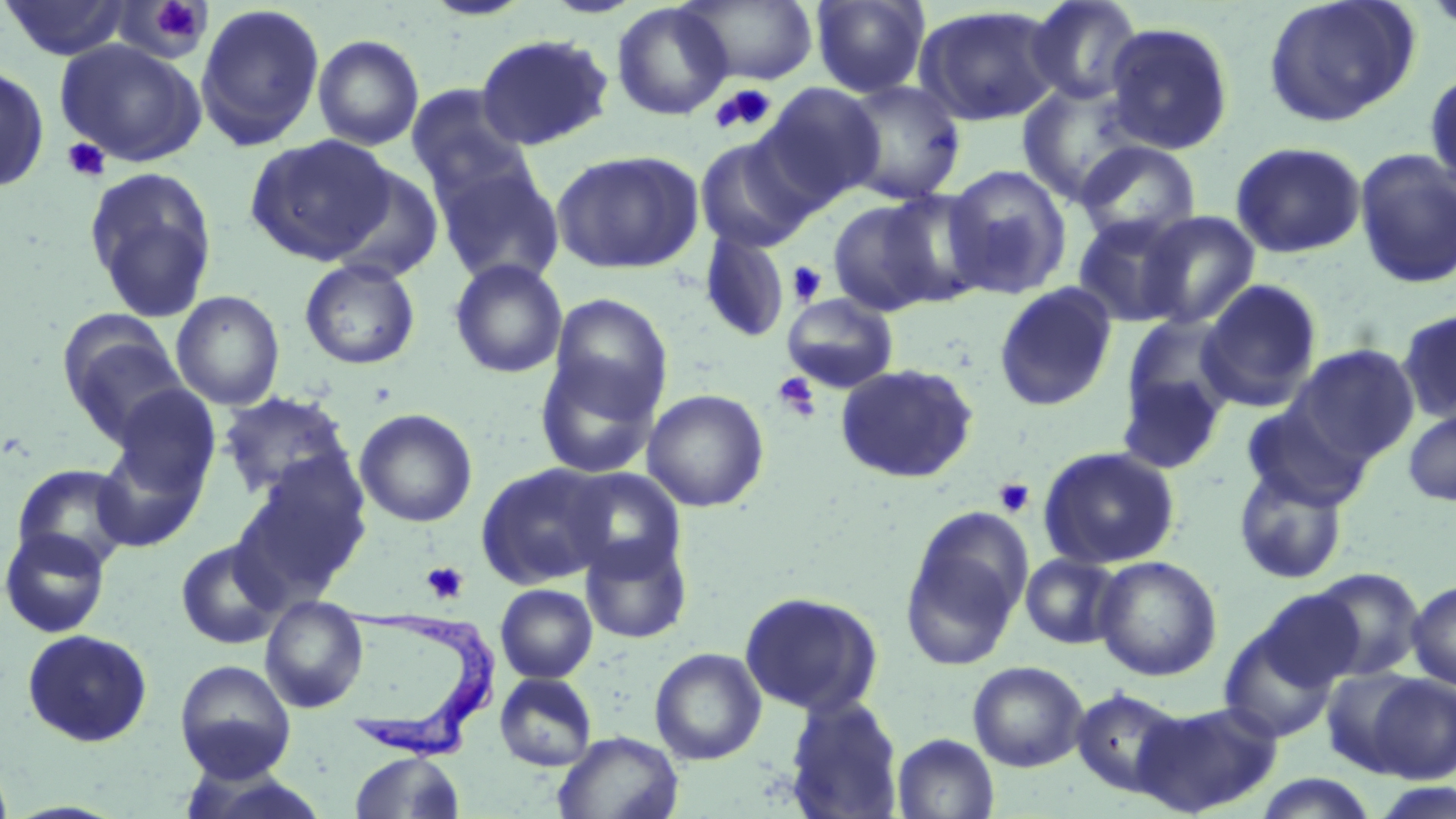 Approximate bounding boxes as (x1, y1, x2, y2) in pixels. Trypanosoma brucei locations: (341, 605, 500, 767). Uninfected red blood cell locations: (2, 0, 130, 60), (421, 0, 535, 21), (682, 0, 819, 85), (811, 0, 929, 98), (1024, 0, 1144, 105), (1262, 0, 1421, 128), (116, 2, 211, 62), (611, 2, 734, 121), (195, 3, 326, 150), (914, 6, 1063, 127), (1103, 21, 1235, 155), (475, 33, 614, 150), (313, 34, 425, 150), (54, 40, 206, 166), (0, 63, 49, 193), (1425, 69, 1456, 191), (840, 80, 966, 205), (1017, 81, 1148, 206), (756, 82, 885, 209), (406, 84, 532, 199), (245, 135, 395, 265), (694, 135, 818, 254), (1074, 140, 1201, 248), (1229, 141, 1366, 259), (1353, 148, 1456, 290), (550, 149, 705, 274), (434, 161, 565, 288), (943, 164, 1073, 299), (329, 165, 445, 283), (84, 167, 217, 321), (879, 189, 992, 308), (827, 198, 944, 317), (1136, 210, 1261, 329), (1071, 213, 1195, 328), (699, 230, 790, 343), (299, 258, 421, 370), (449, 258, 568, 378), (1195, 279, 1322, 411), (994, 282, 1118, 412), (170, 290, 285, 410), (782, 292, 899, 393), (549, 294, 672, 418), (1397, 307, 1456, 423), (61, 318, 189, 441), (1115, 320, 1236, 471), (1287, 344, 1420, 464), (534, 353, 662, 479), (836, 362, 978, 484), (110, 385, 221, 498), (642, 388, 769, 512), (218, 391, 354, 500), (1239, 401, 1373, 512), (1402, 407, 1456, 506), (354, 408, 478, 527), (91, 441, 209, 552), (1038, 445, 1181, 569), (233, 459, 372, 602), (475, 462, 615, 588), (1233, 463, 1350, 586), (11, 464, 135, 570), (899, 506, 1033, 671), (0, 527, 111, 638), (579, 532, 692, 645), (176, 539, 286, 650), (1020, 553, 1124, 649), (1093, 555, 1222, 681), (1307, 567, 1425, 682), (1407, 579, 1456, 691), (495, 583, 597, 683), (1251, 587, 1366, 692), (739, 590, 882, 716), (260, 595, 368, 712), (1218, 620, 1342, 746), (21, 629, 153, 747), (649, 647, 766, 765), (175, 659, 296, 780), (967, 661, 1088, 771), (1321, 667, 1427, 776), (495, 673, 597, 771), (1367, 674, 1456, 783), (1070, 688, 1189, 798), (785, 696, 904, 818), (1133, 699, 1282, 817), (553, 731, 683, 818), (892, 733, 999, 819), (349, 752, 464, 819), (177, 765, 331, 818), (1252, 772, 1379, 818), (1371, 779, 1456, 819). Platelet locations: (153, 1, 198, 35), (711, 83, 778, 134), (62, 137, 110, 182), (787, 260, 827, 307), (773, 371, 821, 422), (993, 478, 1035, 518), (421, 560, 470, 606). Slide-level diagnosis: Trypanosoma brucei. May-Grünwald-Giemsa stain. Captured at 1000x magnification. Thin blood film. Image is 1456×819 pixels. Single field of view. Light microscopy.